Locate every Plasmodium ovale-infected red blood cell.
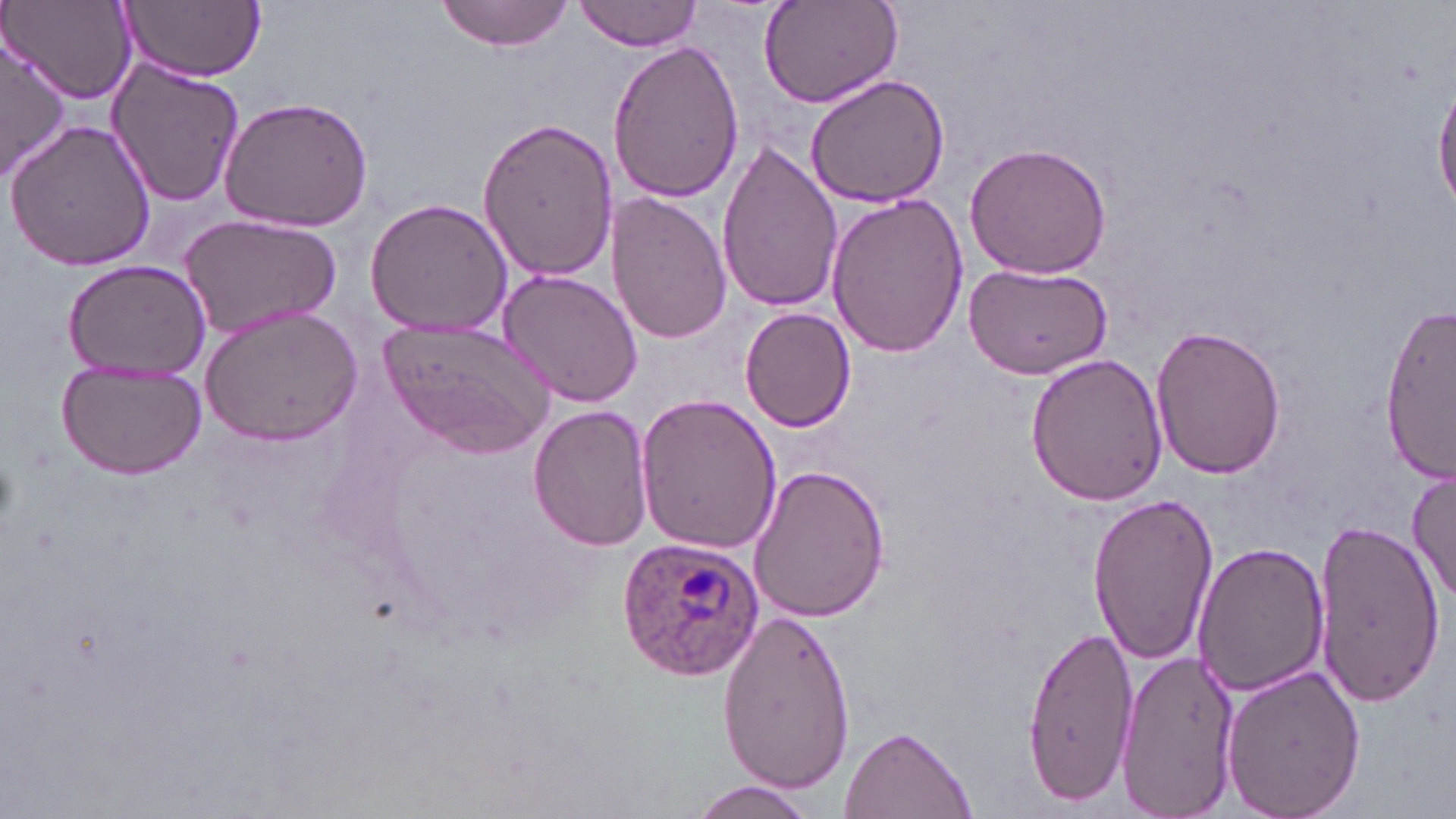

Approximate bounding boxes as [x1, y1, x2, y2] in pixels.
Plasmodium ovale-infected red blood cells: [615, 538, 768, 683].

Summary:
  - Uninfected red blood cell locations: [119, 0, 266, 81], [434, 0, 576, 51], [756, 0, 902, 110], [6, 1, 138, 104], [576, 1, 701, 52], [3, 33, 72, 177], [608, 39, 745, 207], [103, 55, 246, 207], [804, 73, 951, 209], [1434, 77, 1456, 215], [218, 95, 375, 233], [476, 118, 618, 282], [5, 119, 157, 273], [715, 140, 844, 314], [964, 142, 1112, 280], [825, 191, 970, 357], [606, 194, 729, 345], [363, 197, 515, 339], [179, 213, 342, 339], [62, 260, 211, 383], [963, 263, 1113, 381], [498, 270, 643, 408], [1380, 302, 1455, 482], [199, 305, 364, 445], [739, 307, 857, 433], [381, 319, 552, 456], [1152, 324, 1286, 480], [1026, 354, 1169, 505], [54, 359, 207, 478], [633, 392, 783, 556], [528, 405, 654, 549], [744, 465, 888, 625], [1408, 467, 1456, 607], [1086, 491, 1219, 664], [1312, 515, 1444, 711], [1195, 542, 1330, 696], [717, 608, 858, 795], [1023, 623, 1138, 803], [1115, 649, 1238, 816], [1218, 663, 1366, 819], [841, 727, 974, 817], [684, 782, 819, 819]
  - Slide-level diagnosis: Plasmodium ovale
  - Image size: 1456×819 pixels
  - Stain: May-Grünwald-Giemsa
  - Modality: light microscopy
  - Preparation: thin blood smear
  - Magnification: 1000x
  - Field of view: one of a larger specimen